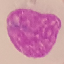

Malaria status: uninfected. Thin blood smear. Photographed with a smartphone camera at the microscope eyepiece. Cell patch, automatically extracted from a larger field of view and resized to 64 × 64 pixels. Giemsa-stained preparation.